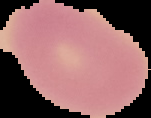

Image is 151×118 pixels. From a thin blood smear. Result: no malaria parasites detected. Cell region segmented out of the field of view; the surrounding area is masked to black.